Assess the morphology of the erythrocytes.
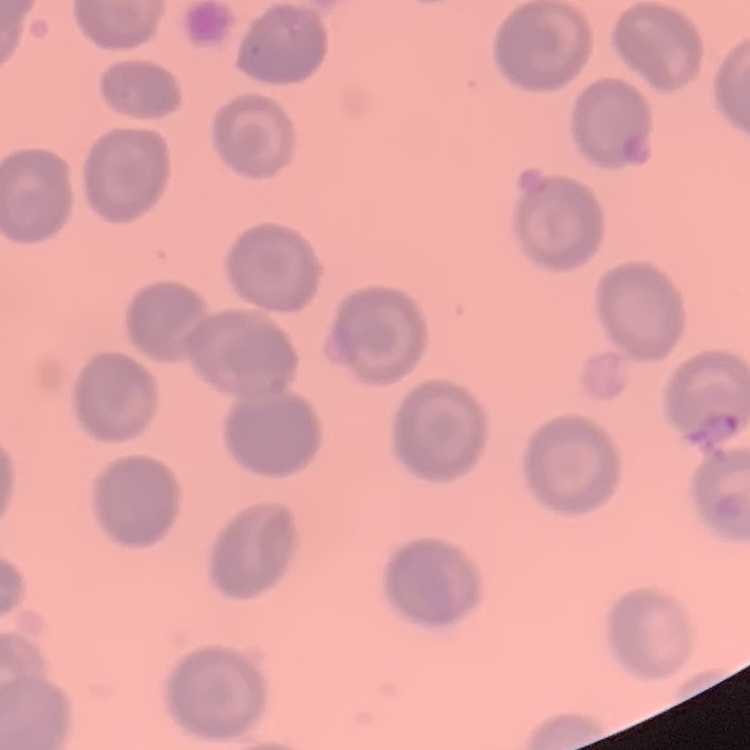
They show no rouleaux formation.

One tile cut from a larger photomicrograph. Stained with either Field's or Giemsa. Thin peripheral smear.